Locate every malaria parasite and every leukocyte.
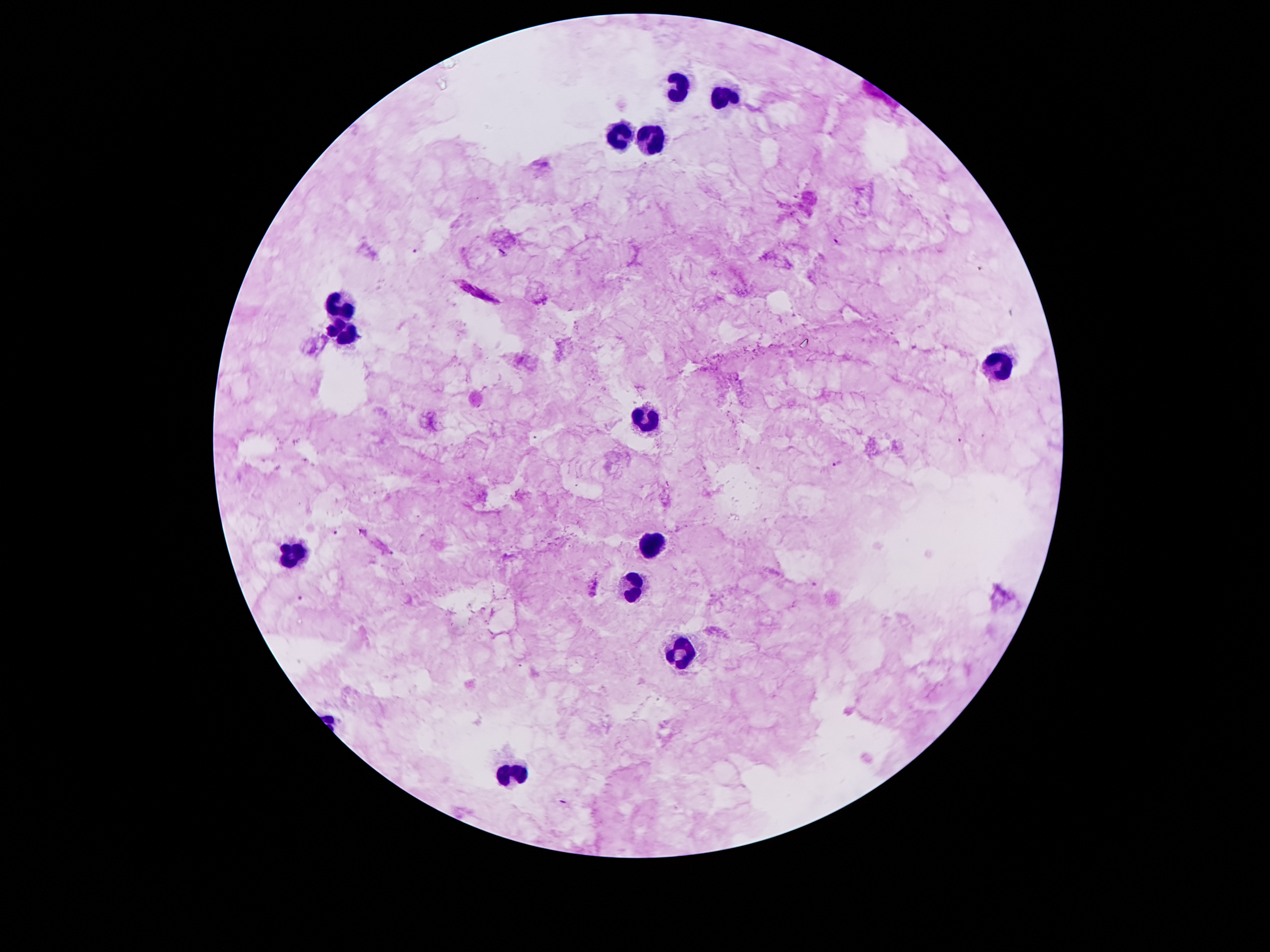
Approximate centers as [x, y] in pixels.
Malaria parasites: [837, 241], [417, 250], [476, 292], [838, 464], [336, 532], [596, 587], [300, 599].
Leukocytes: [679, 88], [721, 95], [618, 135], [654, 144], [337, 306], [345, 333], [992, 367], [643, 426], [654, 546], [297, 554], [633, 590], [683, 649], [513, 774].

preparation: thick blood film
magnification: 100x
image_size: 1270×952 pixels
stain: Giemsa
capture: smartphone through the microscope eyepiece
field_of_view: one from this slide
patient_malaria_status: positive for Plasmodium falciparum